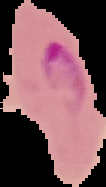

{
  "preparation": "thin blood smear",
  "image_size": "106×187 pixels",
  "image_type": "cell region segmented out of the field of view; surrounding area masked to black",
  "malaria_status": "parasitized"
}